Assess this cell for malaria.
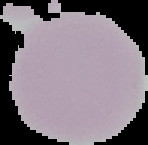

Uninfected.

{
  "image_type": "segmented cell region on a black background",
  "preparation": "thin blood smear",
  "image_size": "148×145 pixels"
}